Describe the morphology of the erythrocytes.
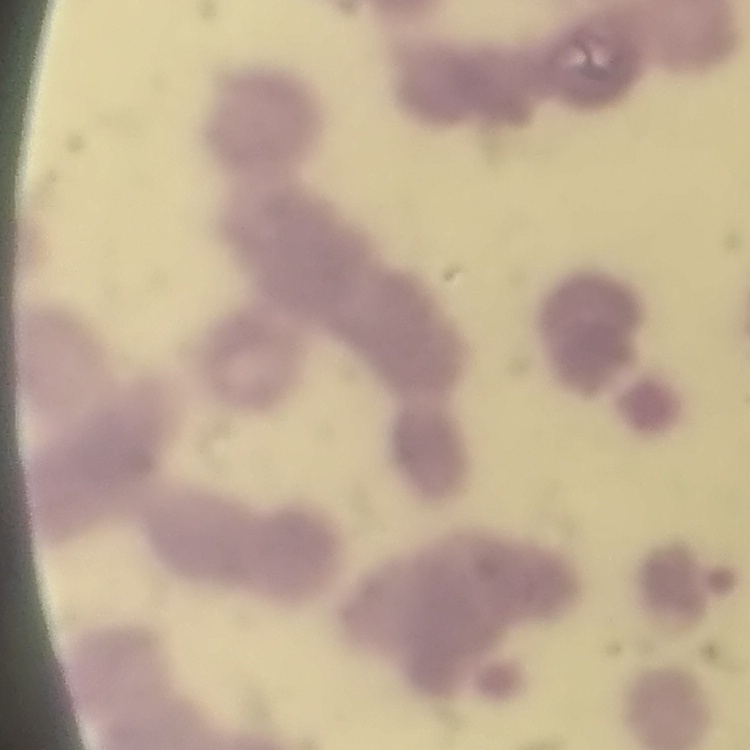

They show rouleaux formation.

Square crop of a larger photomicrograph. Thin blood smear. Field's or Giemsa stain.